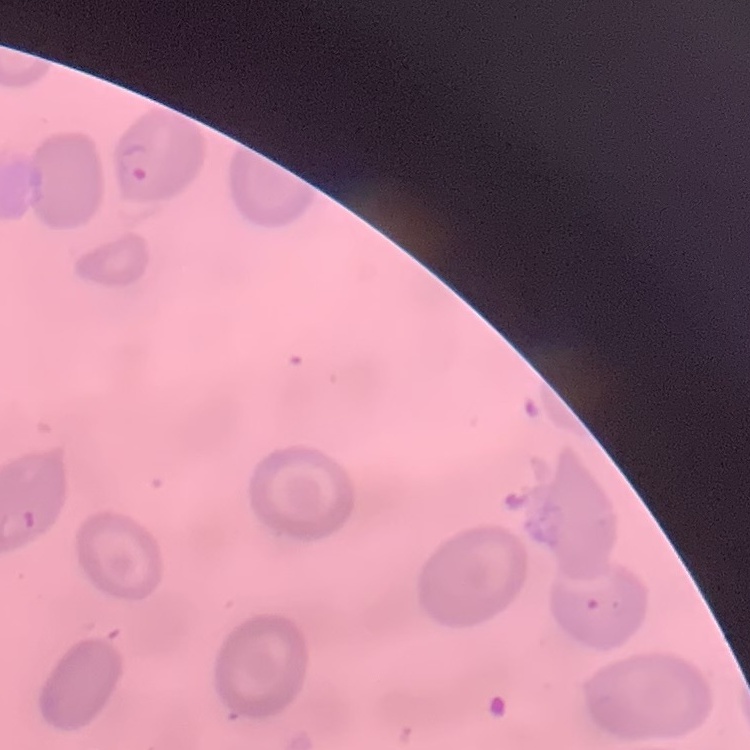

Summary:
  - Red blood cell morphology: no rouleaux formation
  - Stain: Field's or Giemsa
  - Preparation: thin blood smear
  - Image type: one tile cut from a larger photomicrograph